Assess this cell for malaria.
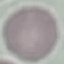
It is uninfected.

stain: Giemsa
image_type: automatically extracted cell patch, resized to 64 × 64 pixels
preparation: thin blood film
capture: smartphone through the microscope eyepiece